Report the malaria status of this cell.
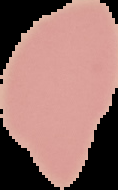
Uninfected.

Summary:
  - Preparation: thin blood film
  - Image type: segmented cell region with the area outside set to black
  - Image size: 118×190 pixels